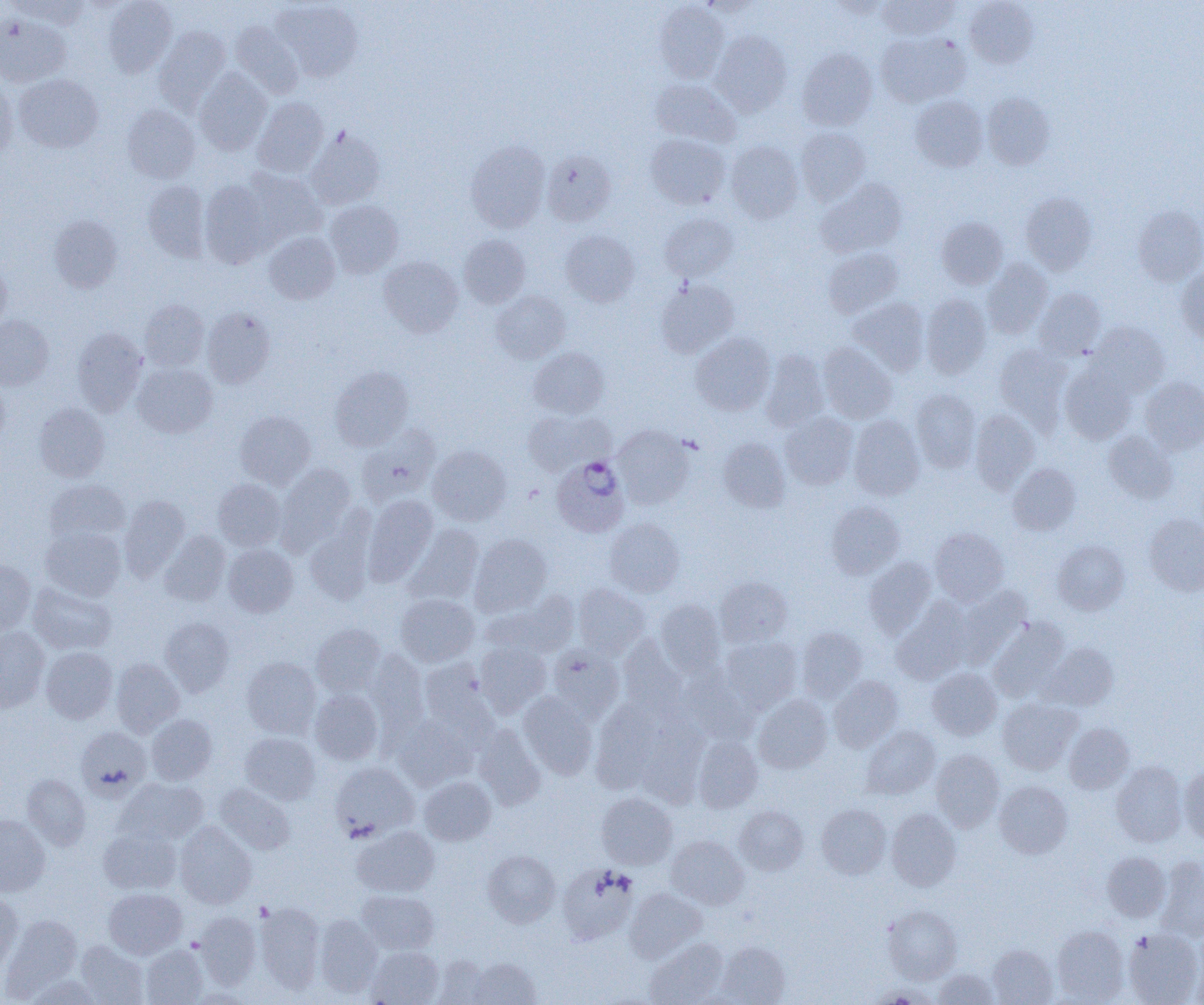
slide-level diagnosis = Plasmodium ovale
magnification = 1000x
uninfected red blood cell locations = approximate bounding boxes as (x1,y1)-(x2,y2) corner pairs in pixels: (7,0)-(90,28), (103,0)-(177,77), (876,0)-(959,41), (964,0)-(1039,68), (271,1)-(363,82), (655,1)-(729,83), (825,1)-(894,19), (0,14)-(71,86), (231,22)-(304,97), (154,26)-(230,112), (710,31)-(792,116), (876,32)-(970,107), (797,48)-(877,131), (194,68)-(271,156), (14,74)-(104,152), (650,79)-(741,147), (0,80)-(17,161), (982,93)-(1055,170), (910,95)-(988,171), (253,97)-(328,178), (123,104)-(200,183), (796,127)-(870,205), (306,129)-(385,209), (646,134)-(730,209), (466,140)-(550,232), (725,141)-(803,222), (541,149)-(616,226), (241,168)-(326,245), (817,179)-(907,257), (200,180)-(275,267), (143,181)-(210,262), (1020,192)-(1097,274), (324,200)-(404,278), (1133,205)-(1204,285), (660,212)-(739,282), (49,215)-(123,293), (937,216)-(1007,288), (561,230)-(639,306), (263,232)-(340,304), (458,234)-(530,308), (823,248)-(903,318), (379,256)-(463,337), (983,259)-(1052,339), (0,260)-(11,333), (1176,267)-(1204,346), (656,280)-(739,358), (1034,288)-(1105,359), (491,290)-(571,363), (921,294)-(991,378), (848,298)-(930,375), (140,300)-(209,370), (202,307)-(275,388), (0,315)-(54,390), (1087,321)-(1169,397), (72,327)-(147,416), (691,333)-(775,415), (818,343)-(897,423), (994,344)-(1071,430), (529,347)-(609,418), (760,351)-(829,431), (132,363)-(217,438), (1060,363)-(1137,444), (330,367)-(414,451), (1140,376)-(1204,454), (0,378)-(10,450), (910,389)-(981,472), (34,403)-(110,482), (970,409)-(1039,493), (523,410)-(605,475), (235,411)-(315,489), (780,411)-(858,489), (848,416)-(925,500), (357,425)-(440,505), (613,425)-(693,509), (1103,431)-(1178,503), (719,438)-(791,512), (428,445)-(511,525), (276,463)-(355,553), (1008,463)-(1081,535), (213,479)-(286,551), (45,480)-(130,545), (119,495)-(190,581), (363,495)-(438,584), (827,501)-(904,579), (1144,514)-(1204,596), (605,517)-(684,597), (304,518)-(374,606), (407,524)-(484,604), (40,526)-(126,601), (930,528)-(1009,605), (160,531)-(230,605), (470,534)-(552,616), (1053,540)-(1129,615), (224,544)-(298,617), (863,557)-(936,639), (0,558)-(35,634), (715,577)-(792,647), (28,582)-(116,655), (573,583)-(649,658), (954,587)-(1031,667), (484,590)-(579,659), (396,594)-(479,667), (892,599)-(973,684), (655,600)-(725,675), (160,616)-(234,696), (988,618)-(1069,701), (311,624)-(386,696), (0,626)-(49,714), (797,627)-(867,703), (617,635)-(686,718), (721,636)-(802,713), (475,640)-(551,717), (1043,643)-(1118,710), (548,644)-(624,721), (41,647)-(117,723), (366,649)-(429,743), (242,657)-(321,738), (111,658)-(184,737), (419,659)-(496,741), (677,666)-(756,745), (927,668)-(1001,740), (829,676)-(903,752), (310,689)-(383,765), (518,692)-(598,779), (753,694)-(832,773), (998,698)-(1082,775), (590,702)-(663,793), (146,714)-(217,785), (636,715)-(708,808), (391,716)-(473,790), (1064,722)-(1134,794), (473,723)-(545,809), (861,725)-(940,799), (76,726)-(152,801), (240,732)-(320,804), (692,736)-(762,812), (931,749)-(1004,831), (1111,761)-(1187,847), (329,762)-(418,840), (1178,767)-(1204,845), (22,775)-(90,850), (419,776)-(496,845), (117,778)-(208,845), (994,781)-(1073,858), (215,783)-(295,855), (596,793)-(677,869), (816,804)-(891,879), (734,806)-(808,876), (887,808)-(961,891), (0,815)-(51,896), (175,821)-(257,909), (98,825)-(181,894), (352,826)-(439,897), (666,835)-(749,910), (482,850)-(561,926), (1102,851)-(1170,922), (1156,856)-(1204,941), (558,863)-(639,945), (104,888)-(186,959), (625,888)-(706,961), (357,890)-(439,954), (0,891)-(23,972), (255,902)-(325,993), (882,904)-(962,983), (195,911)-(261,989), (3,914)-(82,999), (314,915)-(383,997), (1052,926)-(1129,1003), (1124,929)-(1203,1005), (644,938)-(727,1005), (76,940)-(149,1004), (715,941)-(791,1005), (1191,941)-(1204,1005), (140,944)-(208,1005), (988,945)-(1057,1005), (367,946)-(443,1005), (431,957)-(494,1004), (467,957)-(540,1005), (933,968)-(999,1004), (25,975)-(106,1005)
image size = 1204×1005 pixels
Plasmodium ovale-infected red blood cell locations = approximate bounding boxes as (x1,y1)-(x2,y2) corner pairs in pixels: (553,455)-(630,539)
field of view = single
modality = optical microscopy
preparation = thin blood film